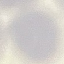

Summary:
  - Result: negative for malaria parasites
  - Preparation: thin blood film
  - Image type: cell patch, automatically extracted from a larger field of view and resized to 64 × 64 pixels
  - Stain: Giemsa
  - Capture: smartphone camera at the microscope eyepiece